Assess this cell for malaria.
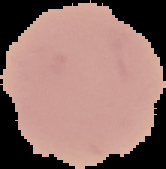
Uninfected.

From a thin blood smear. Cell region segmented out of the field of view; the surrounding area is masked to black. Image is 166×169 pixels.